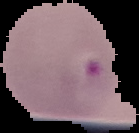

Segmented cell region on a black background. Result: Plasmodium parasites detected. From a thin blood film. Image is 139×133 pixels.